Comment on the morphology of the erythrocytes.
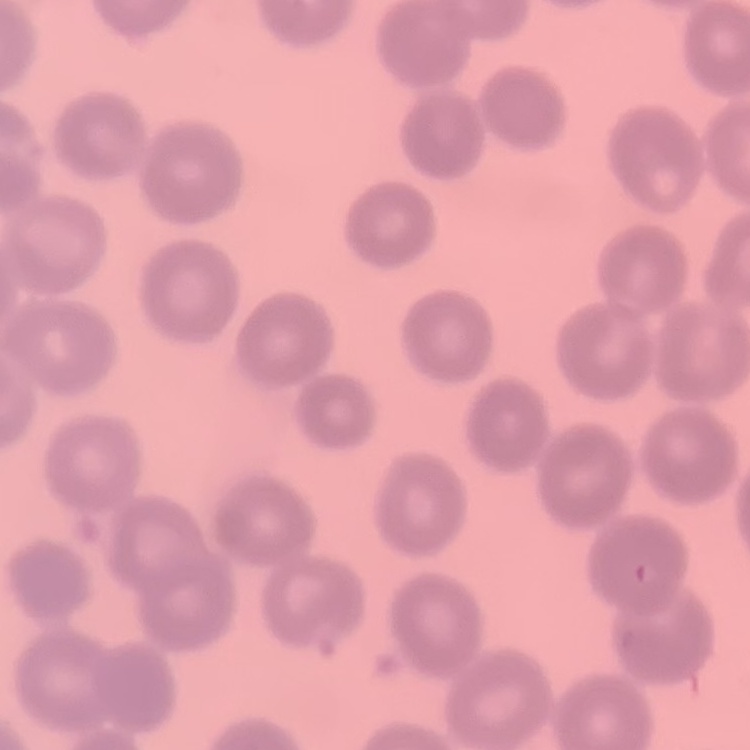

They show no rouleaux formation.

preparation: thin blood smear
stain: Field's or Giemsa
image_type: square crop of a larger photomicrograph